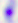

{
  "identification": "Toxoplasma gondii",
  "magnification": "400x",
  "modality": "micrograph"
}